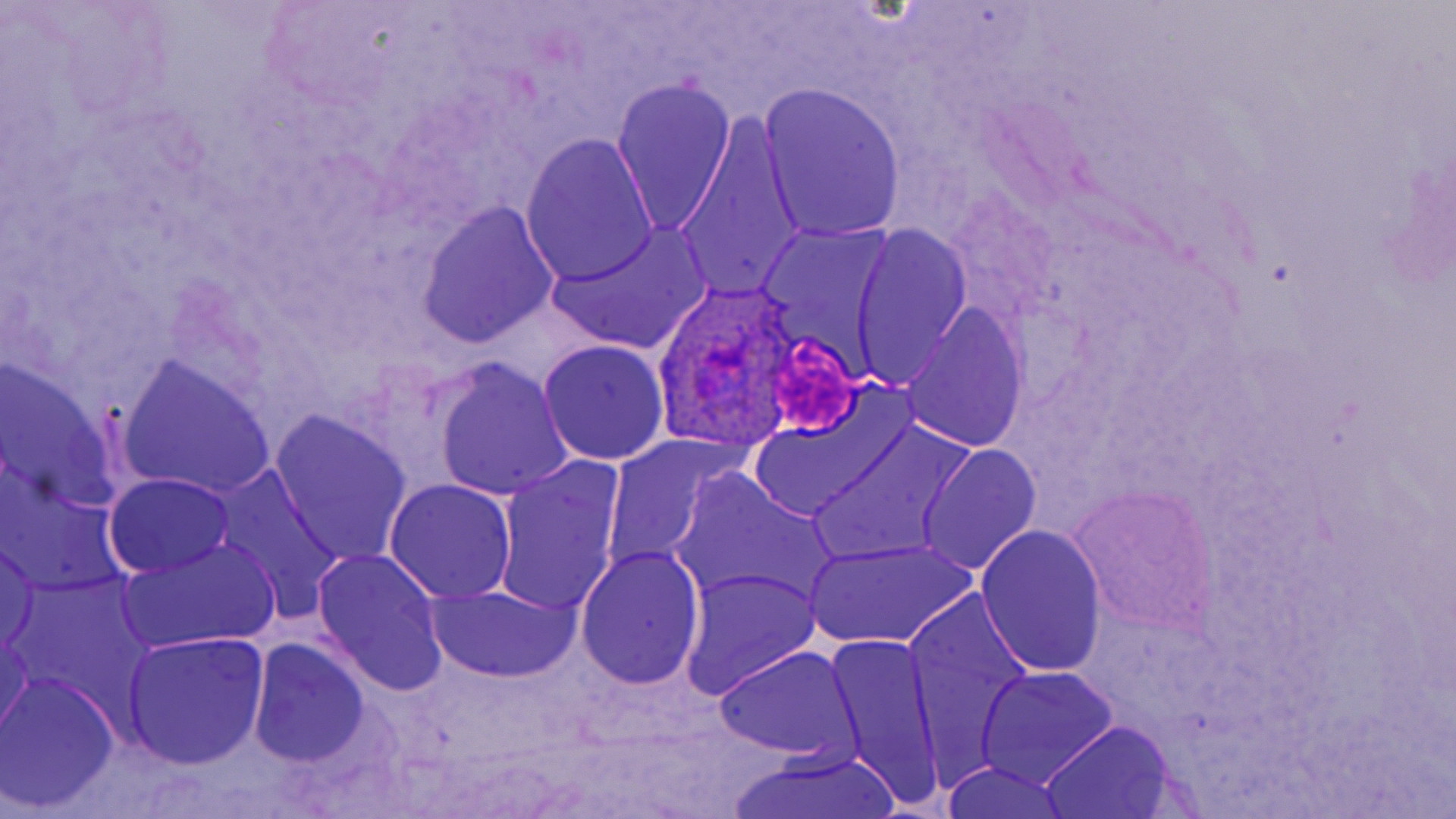
Approximate bounding boxes as (x1, y1, x2, y2) in pixels. Plasmodium ovale-infected red blood cell locations: (657, 279, 803, 452). Uninfected red blood cell locations: (612, 77, 737, 235), (759, 83, 907, 244), (671, 112, 806, 307), (521, 134, 659, 288), (416, 202, 558, 347), (545, 223, 710, 356), (850, 224, 972, 388), (900, 305, 1028, 455), (538, 340, 670, 464), (0, 358, 125, 514), (432, 358, 571, 501), (118, 360, 275, 499), (745, 402, 903, 523), (268, 412, 412, 565), (812, 421, 973, 565), (599, 433, 738, 574), (917, 444, 1040, 575), (493, 457, 627, 619), (672, 469, 839, 613), (214, 472, 349, 619), (103, 473, 237, 578), (383, 478, 518, 603), (1072, 487, 1215, 635), (975, 523, 1107, 677), (0, 538, 42, 656), (121, 538, 281, 654), (806, 538, 976, 650), (575, 544, 705, 691), (311, 548, 450, 698), (681, 567, 822, 701), (424, 583, 580, 684), (905, 595, 1040, 783), (0, 622, 33, 744), (119, 631, 269, 769), (823, 632, 947, 811), (248, 638, 372, 767), (713, 646, 863, 763), (975, 666, 1118, 789), (2, 671, 122, 812), (1039, 721, 1180, 817), (728, 745, 905, 819), (939, 763, 1075, 819). Platelet locations: (772, 330, 862, 442). Slide-level diagnosis: Plasmodium ovale. One field of a larger specimen. May-Grünwald-Giemsa-stained preparation. Thin blood film. Image is 1456×819 pixels. Light microscopy. Captured at 1000x magnification.